Report the malaria status of this cell.
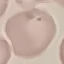
It is uninfected.

Giemsa-stained preparation. Thin smear of blood. Photographed with a smartphone camera at the microscope eyepiece. Cell patch, automatically extracted from a larger field of view and resized to 64 × 64 pixels.